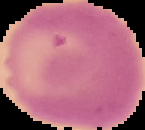
result = no Plasmodium parasites detected
preparation = thin blood smear
image type = segmented cell region with the area outside set to black
image size = 145×130 pixels